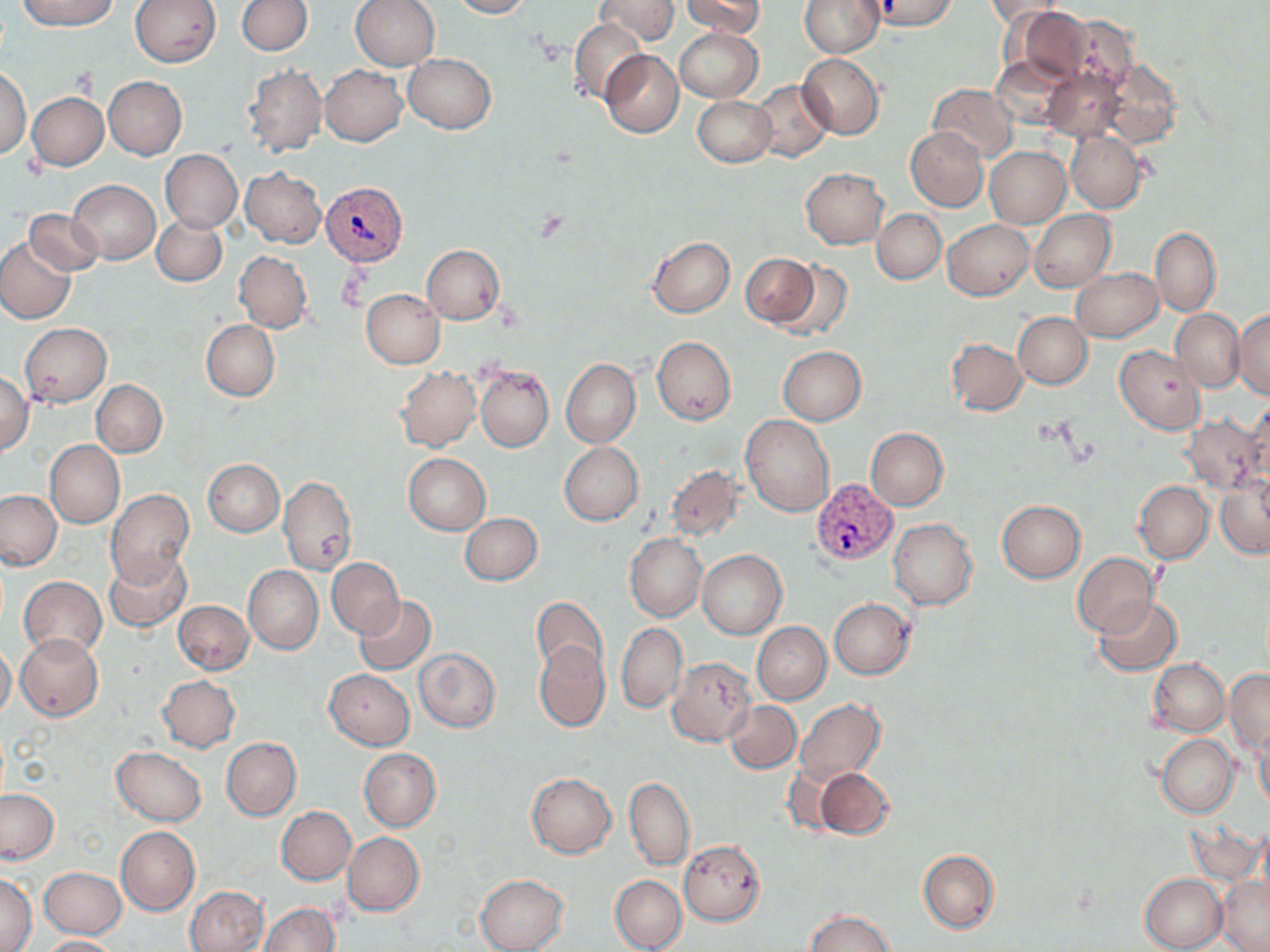
{
  "slide_level_diagnosis": "Plasmodium vivax",
  "modality": "light microscopy",
  "magnification": "1000x",
  "preparation": "thin blood film",
  "field_of_view": "single",
  "image_size": "1270×952 pixels",
  "stain": "May-Grünwald-Giemsa",
  "uninfected_red_blood_cell_locations": "approximate bounding boxes as (x1,y1)-(x2,y2) corner pairs in pixels: (17,0)-(118,30), (131,0)-(221,66), (236,0)-(312,56), (349,0)-(439,71), (450,0)-(531,18), (595,0)-(678,44), (680,0)-(764,39), (800,0)-(884,58), (868,1)-(961,32), (984,1)-(1068,27), (1014,6)-(1094,83), (1060,15)-(1137,93), (569,18)-(645,105), (674,27)-(762,102), (600,50)-(684,138), (404,53)-(495,134), (798,53)-(884,138), (991,55)-(1076,130), (1101,56)-(1184,147), (320,65)-(408,146), (244,66)-(326,157), (0,68)-(31,159), (1043,69)-(1129,143), (104,76)-(186,159), (750,80)-(835,162), (927,84)-(1019,163), (28,92)-(108,170), (693,96)-(776,166), (905,128)-(989,211), (1066,131)-(1146,213), (984,146)-(1070,228), (161,150)-(241,232), (241,167)-(325,248), (801,168)-(887,249), (70,181)-(160,262), (25,209)-(105,276), (872,209)-(946,283), (1030,210)-(1116,291), (153,213)-(227,286), (943,218)-(1034,301), (1150,227)-(1222,316), (648,237)-(735,318), (0,239)-(74,324), (422,245)-(504,323), (235,251)-(311,332), (741,252)-(821,328), (774,260)-(851,338), (1071,268)-(1162,342), (361,289)-(445,368), (1231,308)-(1270,400), (1172,309)-(1243,393), (1013,312)-(1092,389), (201,320)-(280,401), (20,323)-(111,407), (652,336)-(736,425), (948,338)-(1027,415), (1116,344)-(1206,434), (777,346)-(866,425), (561,359)-(640,447), (476,366)-(553,451), (395,367)-(480,452), (0,373)-(33,454), (92,380)-(167,457), (1243,401)-(1270,483), (741,415)-(834,516), (1180,415)-(1266,496), (867,428)-(948,510), (45,440)-(125,528), (560,443)-(643,525), (403,454)-(490,536), (202,459)-(284,536), (666,466)-(744,543), (279,477)-(357,574), (1216,478)-(1270,559), (1134,481)-(1213,563), (0,490)-(63,571), (105,490)-(195,588), (997,500)-(1086,582), (460,512)-(543,586), (889,518)-(977,610), (625,533)-(706,622), (698,550)-(786,639), (1072,552)-(1159,637), (104,553)-(191,632), (327,558)-(404,638), (243,565)-(323,654), (20,576)-(107,658), (353,595)-(437,674), (531,597)-(608,678), (1093,597)-(1183,676), (829,598)-(914,679), (167,601)-(246,749), (172,601)-(253,675), (752,622)-(831,704), (616,623)-(686,712), (16,633)-(104,720), (534,640)-(610,732), (0,644)-(16,720), (413,648)-(500,733), (667,657)-(756,747), (1149,659)-(1231,736), (1225,669)-(1269,754), (325,670)-(414,749), (156,675)-(240,753), (794,699)-(886,785), (724,701)-(801,773), (1254,725)-(1270,816), (1156,734)-(1239,818), (222,737)-(301,820), (111,747)-(206,825), (359,749)-(441,830), (813,766)-(894,840), (526,774)-(617,858), (625,777)-(694,871), (0,790)-(58,863), (276,807)-(356,884), (1184,816)-(1267,887), (116,826)-(200,914), (343,832)-(424,916), (678,839)-(766,926), (918,849)-(999,933), (39,868)-(126,938), (0,873)-(37,952), (1139,873)-(1228,952), (475,874)-(569,952), (610,875)-(686,952), (1215,876)-(1270,952), (185,885)-(268,951), (258,903)-(340,952), (804,911)-(898,952), (39,936)-(120,952)",
  "plasmodium_vivax_infected_red_blood_cell_locations": "approximate bounding boxes as (x1,y1)-(x2,y2) corner pairs in pixels: (320,180)-(405,266), (811,479)-(896,566)"
}